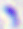
Micrograph. Toxoplasma gondii is seen. 400x magnification.